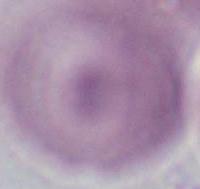
Captured at 1000x magnification. An erythrocyte is seen. Photomicrograph.